Give the position of every malaria parasite and every leukocyte.
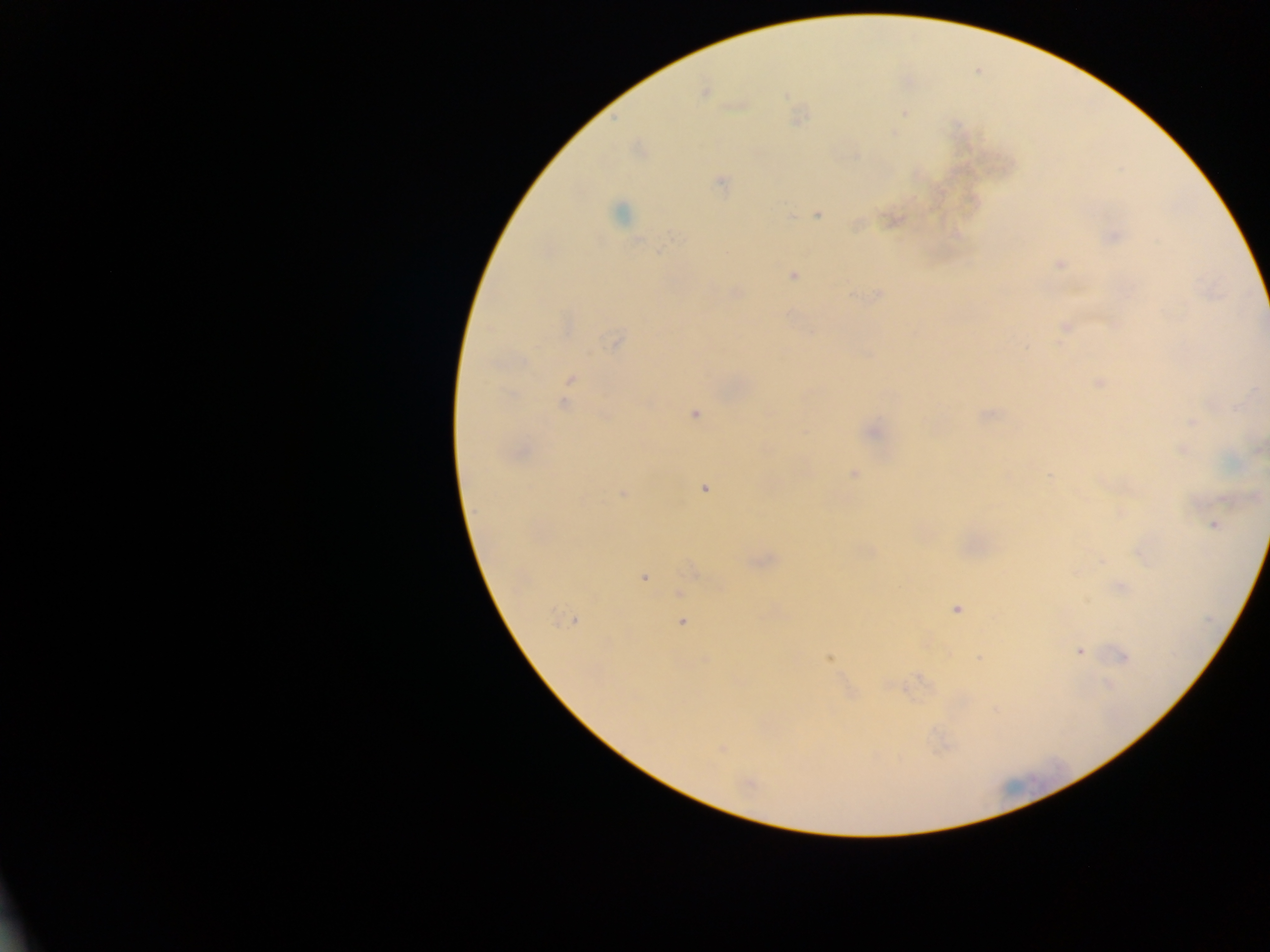

Approximate centers as x y in pixels.
Malaria parasites: 704 91; 739 104; 904 113; 797 117; 721 183; 619 213; 817 214; 788 216; 891 219; 1112 235; 1059 264; 793 276; 735 293; 877 295; 1066 328; 617 340; 570 379; 1099 382; 567 388; 565 402; 694 414; 986 415; 1192 422; 871 430; 1257 448; 1182 449; 519 451; 852 473; 704 487; 622 494; 1213 525; 1141 551; 1101 560; 759 561; 692 570; 643 576; 1120 587; 679 593; 956 608; 572 620; 681 621; 1079 651; 1122 656; 828 658; 979 658; 916 680; 722 749; 750 785.
No leukocytes observed.

{
  "country": "Ghana",
  "image_size": "1270×952 pixels",
  "preparation": "thick blood film",
  "capture": "mobile-phone photograph through a microscope",
  "field_of_view": "single"
}